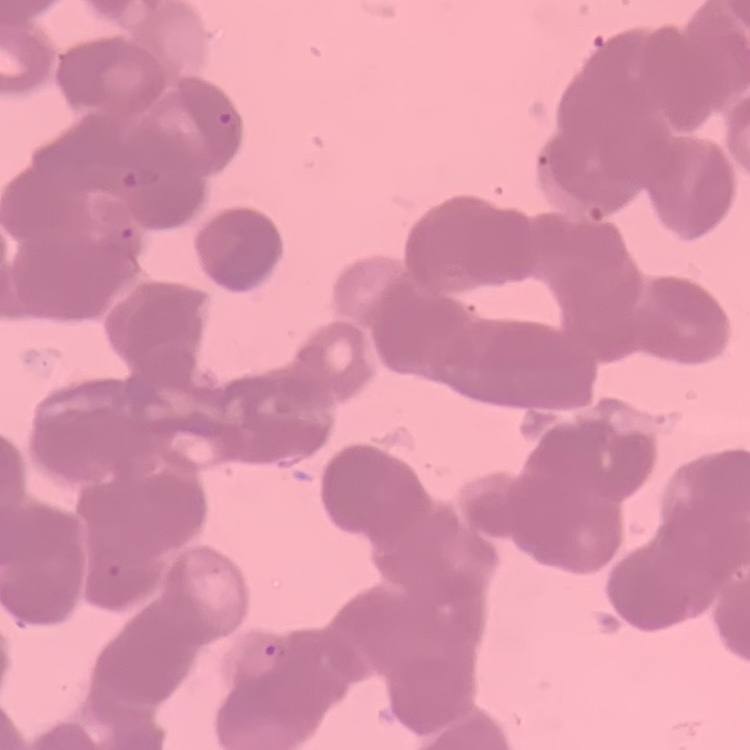
Summary:
  - Red blood cell morphology: rouleaux formation
  - Image type: square crop of a larger photomicrograph
  - Preparation: thin blood smear
  - Stain: Field's or Giemsa